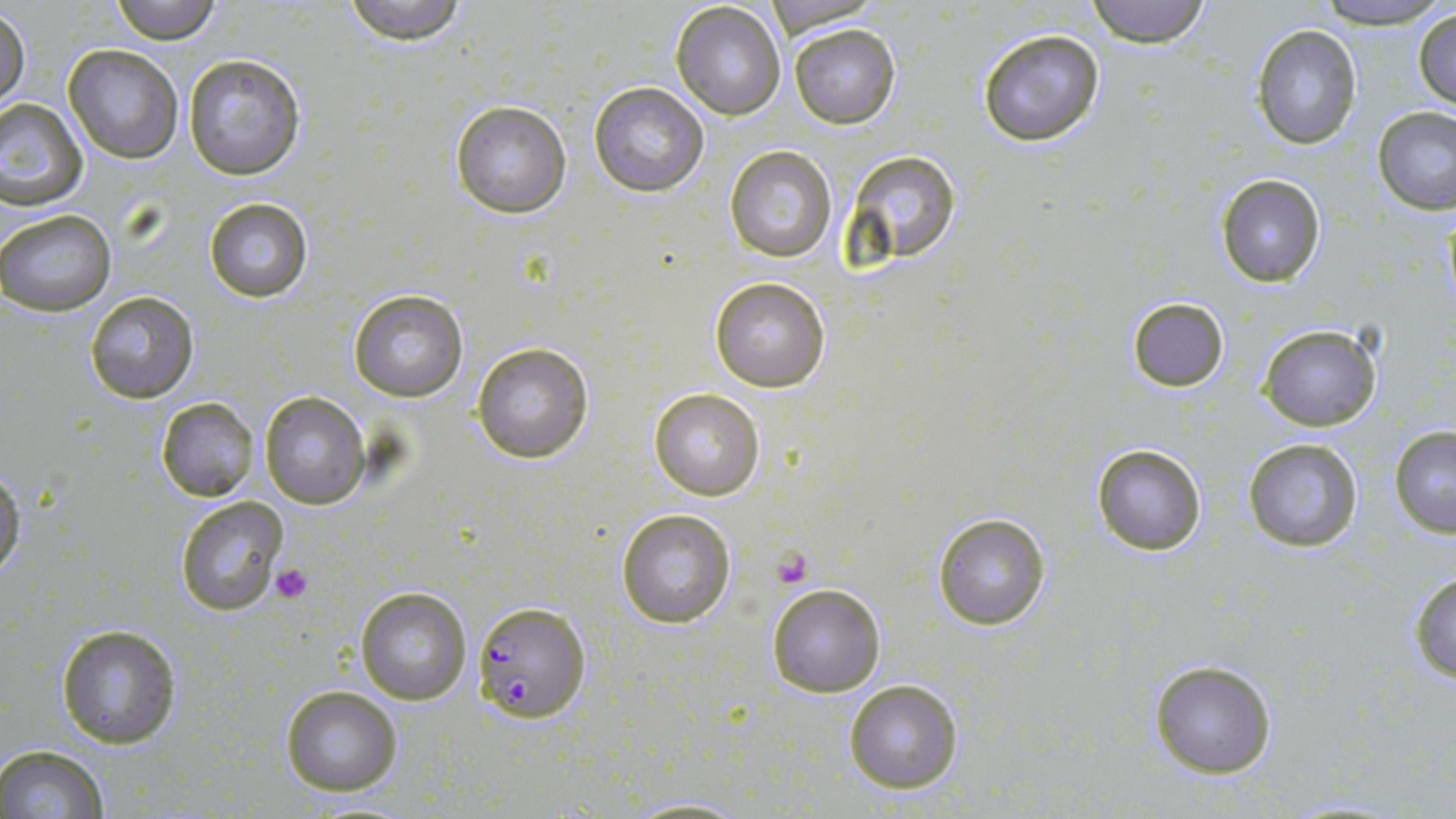
Summary:
  - Coordinate format: approximate bounding boxes as [x1, y1, x2, y2] in pixels
  - Plasmodium falciparum-infected red blood cell locations: [471, 601, 590, 722]
  - Platelet locations: [774, 548, 813, 588], [269, 564, 312, 604]
  - Uninfected red blood cell locations: [110, 0, 221, 44], [339, 0, 473, 45], [761, 0, 886, 35], [1084, 0, 1214, 48], [1317, 0, 1442, 26], [670, 2, 787, 119], [1, 6, 30, 112], [1413, 6, 1456, 110], [1251, 23, 1362, 150], [790, 24, 900, 129], [977, 29, 1106, 148], [62, 44, 184, 164], [182, 53, 306, 180], [589, 82, 710, 197], [1, 98, 89, 209], [449, 99, 573, 219], [1373, 105, 1455, 216], [724, 145, 837, 262], [846, 149, 960, 262], [1216, 174, 1327, 288], [202, 197, 313, 302], [0, 209, 116, 316], [709, 276, 830, 391], [347, 287, 469, 404], [84, 290, 198, 405], [1127, 296, 1229, 392], [1256, 322, 1382, 431], [472, 343, 594, 464], [649, 389, 764, 499], [260, 391, 369, 509], [155, 397, 259, 501], [1389, 426, 1456, 537], [1243, 436, 1365, 554], [1091, 443, 1206, 557], [0, 467, 24, 583], [173, 495, 290, 617], [615, 507, 737, 629], [930, 512, 1052, 629], [1407, 570, 1456, 683], [767, 582, 885, 697], [354, 585, 471, 705], [54, 624, 184, 749], [1146, 658, 1278, 778], [843, 679, 965, 795], [279, 685, 404, 798], [0, 745, 111, 819], [616, 794, 755, 818]
  - Slide-level diagnosis: Plasmodium falciparum
  - Magnification: 1000x
  - Preparation: thin blood film
  - Stain: May-Grünwald-Giemsa
  - Image size: 1456×819 pixels
  - Modality: light microscopy
  - Field of view: single